Report the malaria status of this cell.
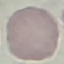
It is uninfected.

stain = Giemsa
capture = smartphone camera at the microscope eyepiece
image type = cell patch, automatically extracted from a larger field of view and resized to 64 × 64 pixels
preparation = thin smear